Describe the morphology of the erythrocytes.
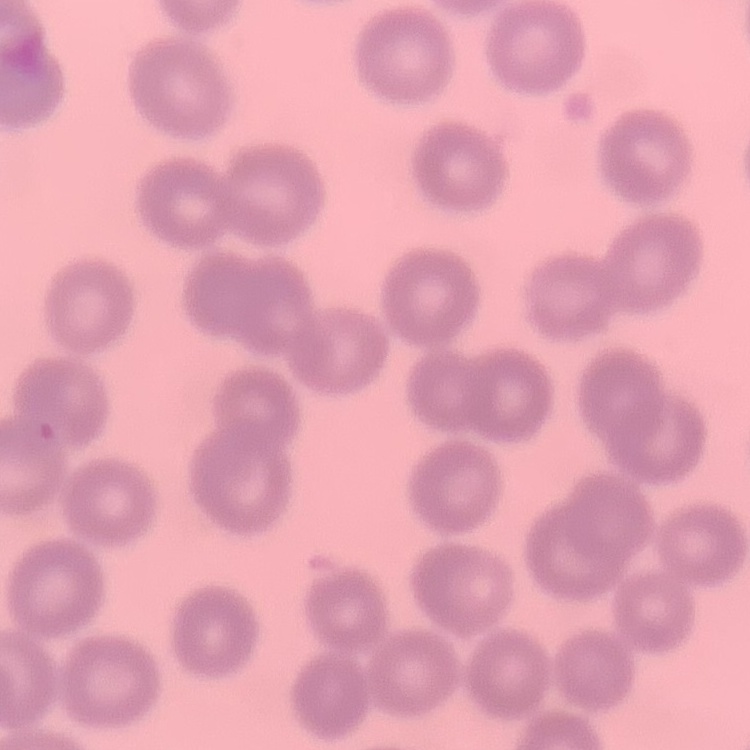
No rouleaux formation.

Summary:
  - Preparation: thin blood film
  - Image type: square crop of a larger photomicrograph
  - Stain: Field's or Giemsa